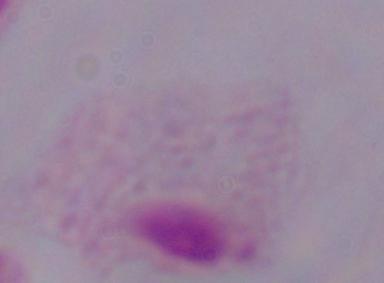

A trichomonad is shown. Captured at 1000x magnification. Photomicrograph.